Describe the morphology of the red blood cells.
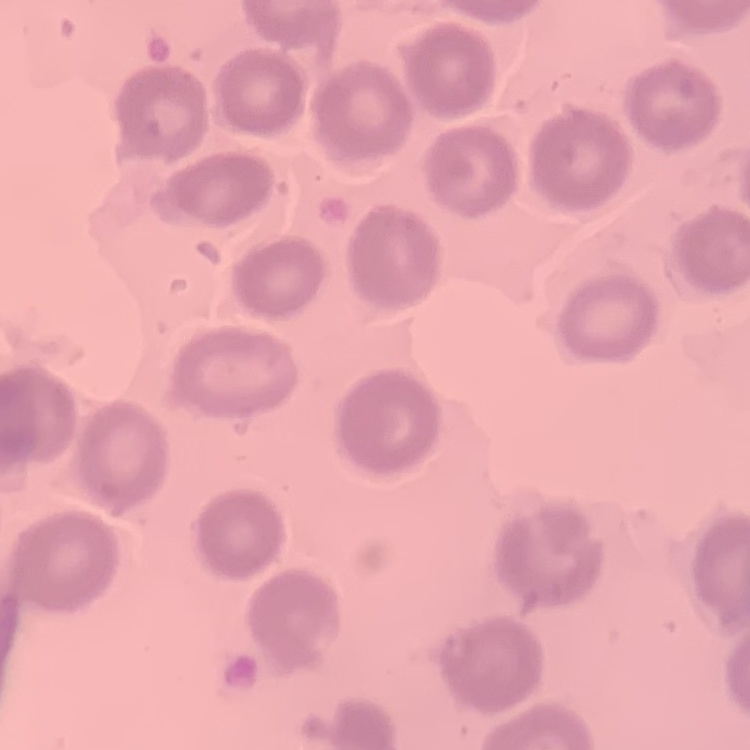

They show no rouleaux formation.

image type = one tile cut from a larger photomicrograph
stain = Field's or Giemsa
preparation = thin blood smear